Name the cell type shown.
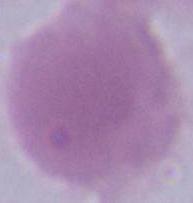
An erythrocyte.

modality = photomicrograph
magnification = 1000x